Locate every Plasmodium falciparum-infected red blood cell.
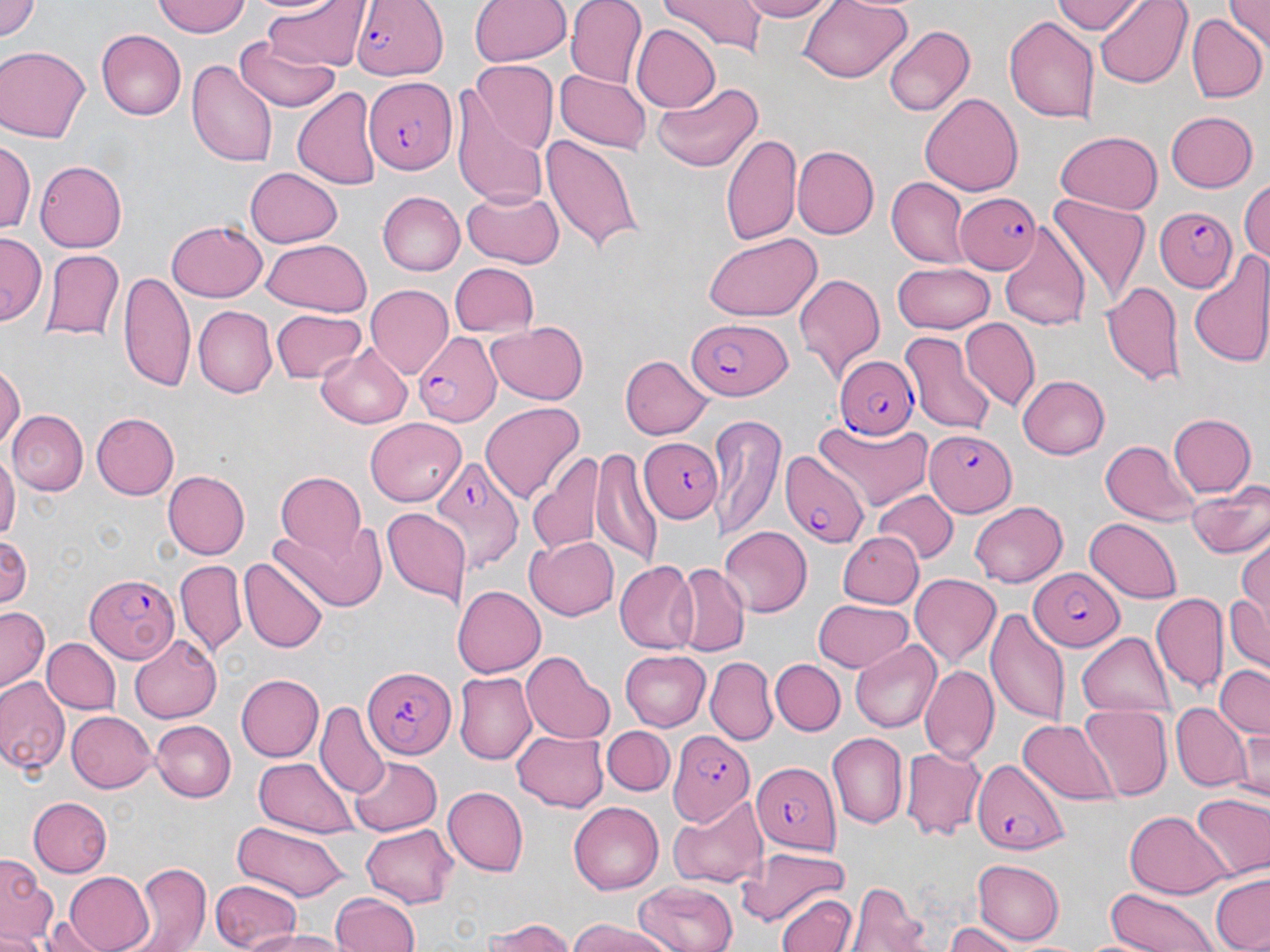
Approximate bounding boxes as (x1,y1)-(x2,y2) corner pairs in pixels.
Plasmodium falciparum-infected red blood cells: (350,0)-(448,79), (363,76)-(454,173), (957,193)-(1041,273), (1155,207)-(1239,292), (685,322)-(791,399), (412,332)-(500,425), (835,354)-(921,440), (925,433)-(1017,517), (640,437)-(724,521), (779,450)-(868,548), (431,452)-(524,575), (1028,569)-(1123,649), (83,573)-(180,664), (361,667)-(452,758), (667,731)-(752,824), (971,757)-(1071,854), (752,760)-(840,855).

slide_level_diagnosis: Plasmodium falciparum
preparation: thin blood smear
uninfected_red_blood_cell_locations: 'approximate bounding boxes as (x1,y1)-(x2,y2) corner pairs in pixels: (0,0)-(42,41), (153,0)-(250,39), (470,0)-(570,67), (566,0)-(648,89), (662,0)-(766,51), (733,0)-(839,22), (797,0)-(913,84), (1053,0)-(1146,34), (1092,0)-(1192,88), (1226,0)-(1270,49), (258,1)-(366,71), (1055,3)-(1175,64), (1004,14)-(1100,124), (1188,14)-(1267,103), (631,23)-(720,113), (884,25)-(975,116), (96,28)-(185,119), (233,37)-(341,113), (2,47)-(91,144), (186,58)-(276,169), (468,61)-(560,153), (556,70)-(651,153), (654,81)-(762,173), (293,86)-(381,192), (919,93)-(1025,196), (453,94)-(551,209), (1166,110)-(1258,192), (1056,131)-(1164,213), (720,132)-(802,247), (542,134)-(646,255), (1,138)-(35,241), (790,145)-(877,238), (35,160)-(129,252), (246,167)-(344,246), (1239,177)-(1270,267), (887,178)-(971,268), (462,188)-(563,268), (375,191)-(465,277), (1048,195)-(1148,307), (166,220)-(266,302), (998,230)-(1089,334), (703,232)-(823,321), (0,235)-(43,323), (261,238)-(372,315), (42,251)-(123,341), (1189,253)-(1270,369), (449,263)-(540,339), (892,264)-(994,332), (119,269)-(195,391), (793,273)-(884,382), (1101,280)-(1185,386), (365,286)-(453,376), (192,305)-(277,397), (269,308)-(367,383), (960,318)-(1038,410), (486,321)-(589,404), (901,330)-(995,432), (318,342)-(415,428), (620,356)-(711,438), (0,365)-(24,456), (1019,374)-(1112,459), (481,400)-(584,505), (7,410)-(84,496), (89,412)-(179,501), (709,414)-(785,541), (1167,414)-(1257,498), (364,416)-(466,504), (817,422)-(933,509), (1103,438)-(1197,526), (594,445)-(657,569), (0,452)-(17,546), (527,452)-(603,555), (165,468)-(250,558), (275,470)-(368,555), (1188,483)-(1270,560), (873,490)-(956,564), (968,500)-(1069,586), (381,506)-(466,605), (1087,517)-(1182,600), (277,525)-(385,611), (718,525)-(814,615), (837,529)-(923,606), (1233,531)-(1270,656), (0,534)-(32,613), (526,534)-(622,619), (240,555)-(328,654), (174,559)-(247,658), (614,560)-(700,653), (673,563)-(748,657), (909,573)-(1002,673), (453,583)-(546,675), (1224,588)-(1270,676), (1153,593)-(1229,693), (814,599)-(915,675), (1,606)-(49,691), (987,610)-(1069,727), (1077,633)-(1175,719), (130,636)-(224,724), (44,637)-(120,714), (851,640)-(942,732), (620,649)-(713,730), (521,650)-(613,741), (706,655)-(777,743), (771,659)-(845,736), (922,663)-(998,761), (1213,664)-(1270,737), (453,672)-(538,764), (236,674)-(324,761), (0,678)-(68,774), (316,702)-(386,795), (1173,703)-(1252,790), (1078,706)-(1171,801), (68,709)-(157,793), (1019,720)-(1116,805), (151,721)-(236,802), (603,723)-(677,796), (1234,723)-(1270,802), (512,730)-(608,811), (825,734)-(906,829), (902,746)-(986,839), (349,754)-(442,835), (255,756)-(356,837), (441,787)-(528,877), (1190,794)-(1270,882), (27,797)-(112,878), (671,798)-(767,889), (569,801)-(664,894), (1124,811)-(1231,900), (231,821)-(352,899), (362,825)-(458,905), (735,846)-(849,927), (1,853)-(52,942), (973,860)-(1065,944), (132,862)-(210,951), (62,870)-(154,952), (1210,874)-(1270,952), (211,878)-(304,952), (635,878)-(739,952), (849,883)-(927,952), (1103,887)-(1219,952), (773,888)-(858,952), (327,890)-(422,952), (44,914)-(106,952), (483,918)-(582,952), (566,918)-(675,952), (944,921)-(1019,952), (0,929)-(48,952), (242,929)-(353,951)'
stain: May-Grünwald-Giemsa
magnification: 1000x
image_size: 1270×952 pixels
field_of_view: one of a larger specimen
modality: optical microscopy